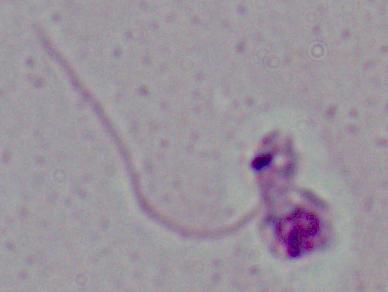
{
  "identification": "Leishmania",
  "modality": "photomicrograph",
  "magnification": "1000x"
}